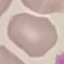

Malaria status: uninfected. Thin smear of blood. Automatically extracted cell patch, resized to 64 × 64 pixels. Giemsa stain. Acquired by smartphone through the microscope eyepiece.